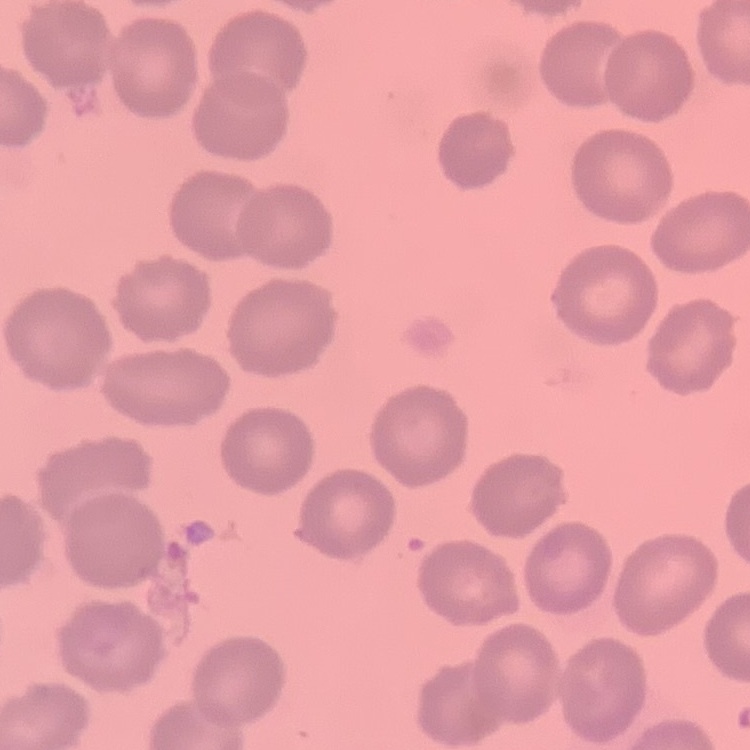

The erythrocytes exhibit no rouleaux formation. Field's or Giemsa stain. Square crop of a larger photomicrograph. Thin blood smear.